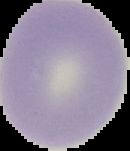 The area outside the segmented cell region is set to black. Image is 130×151 pixels. From a thin blood film. Result: negative for malaria parasites.